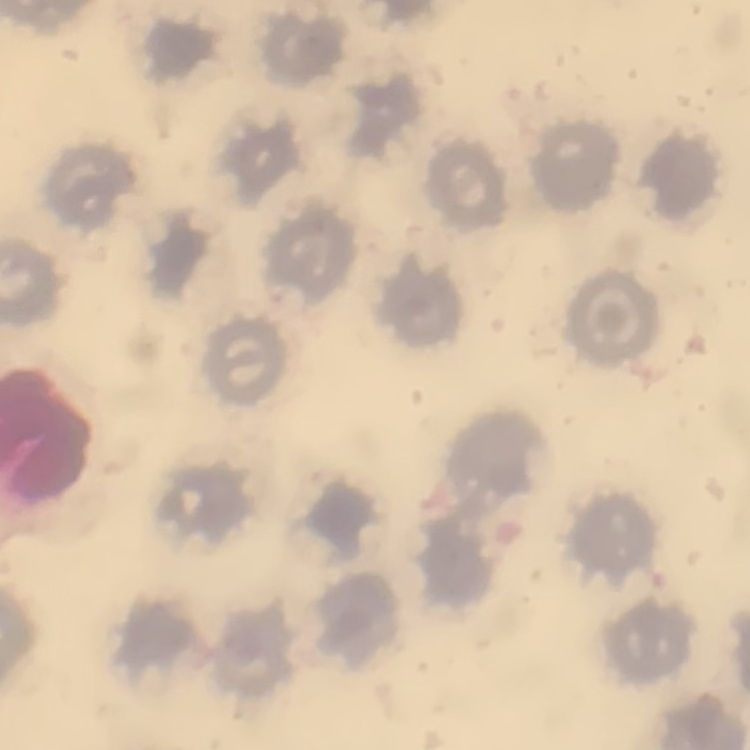

Summary:
  - Erythrocyte morphology: no rouleaux formation
  - Stain: Field's or Giemsa
  - Preparation: thin peripheral smear
  - Image type: one tile cut from a larger photomicrograph